Report the malaria status of this cell.
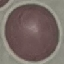
Uninfected.

Thin blood smear. Cell patch, automatically extracted from a larger field of view and resized to 64 × 64 pixels. Giemsa-stained preparation. Acquired by smartphone through the microscope eyepiece.